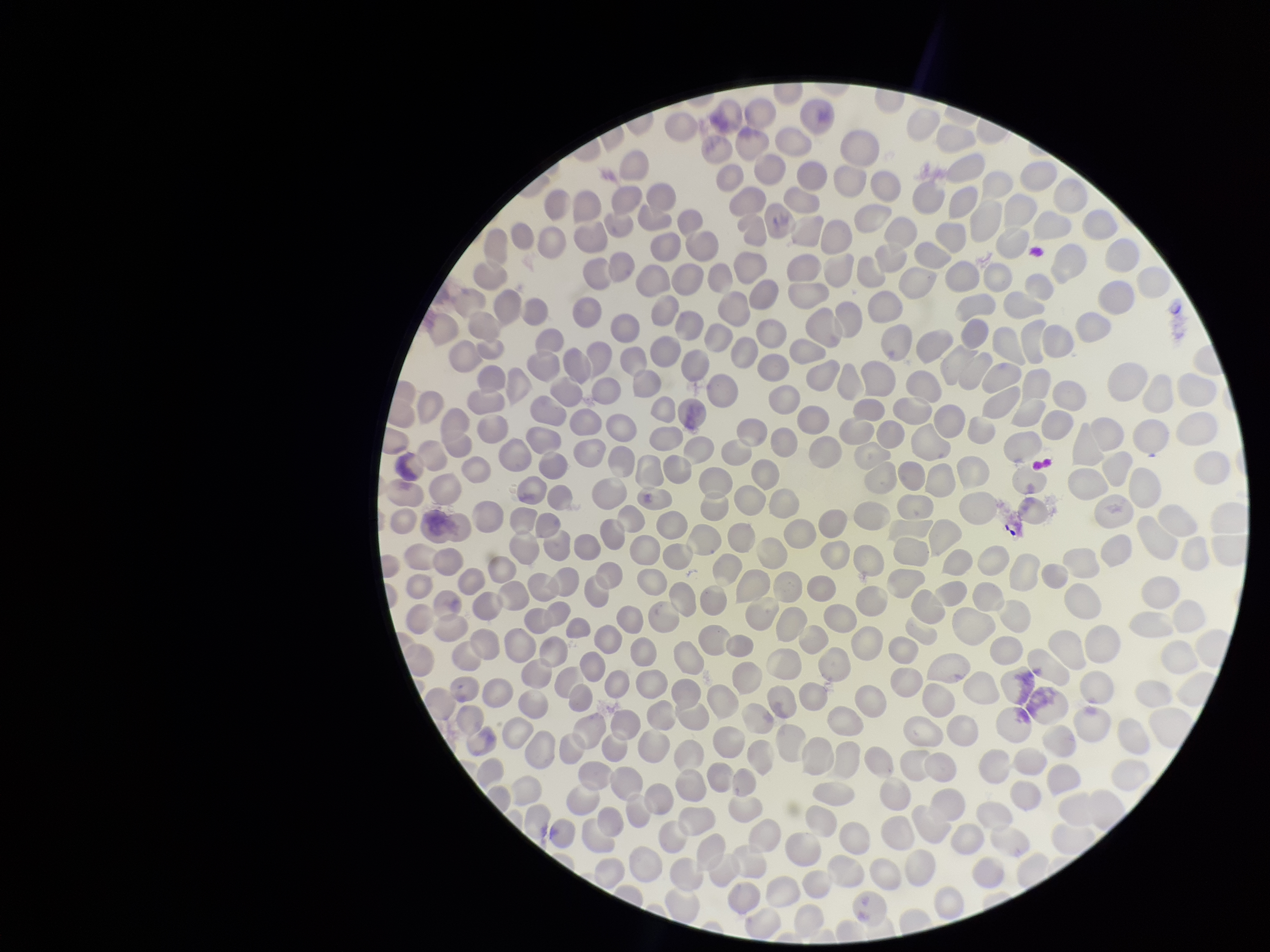

stain = Giemsa
preparation = thin smear
red blood cell count = 299
parasitized red blood cells = none seen
capture = smartphone photograph through the microscope eyepiece
patient malaria status = negative
image size = 1270×952 pixels
parasitized red blood cell count = 0
field of view = one from this slide